Mark where leukocytes are.
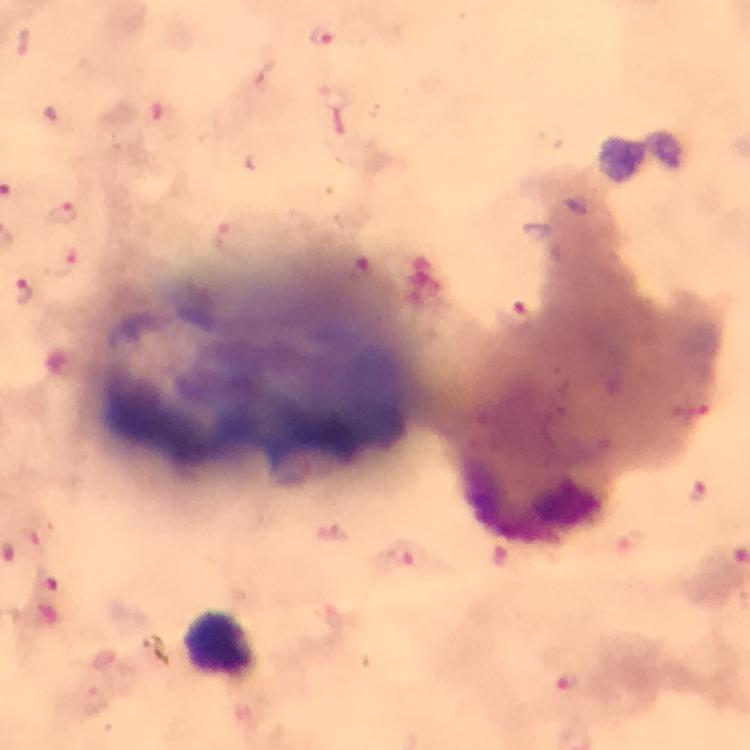
Approximate centers as [x, y] in pixels.
Leukocytes: [222, 645].

Malaria parasite locations: [321, 35], [24, 43], [63, 214], [69, 262], [24, 293], [516, 315], [699, 495], [333, 530], [406, 555], [47, 581], [568, 681]. Image is 750×750 pixels. Photographed through the microscope with a smartphone camera. Immersion oil applied. From a malaria diagnostic workup. At 100x magnification. Cropped region of a single field of view. Giemsa-stained preparation. Thick blood smear.